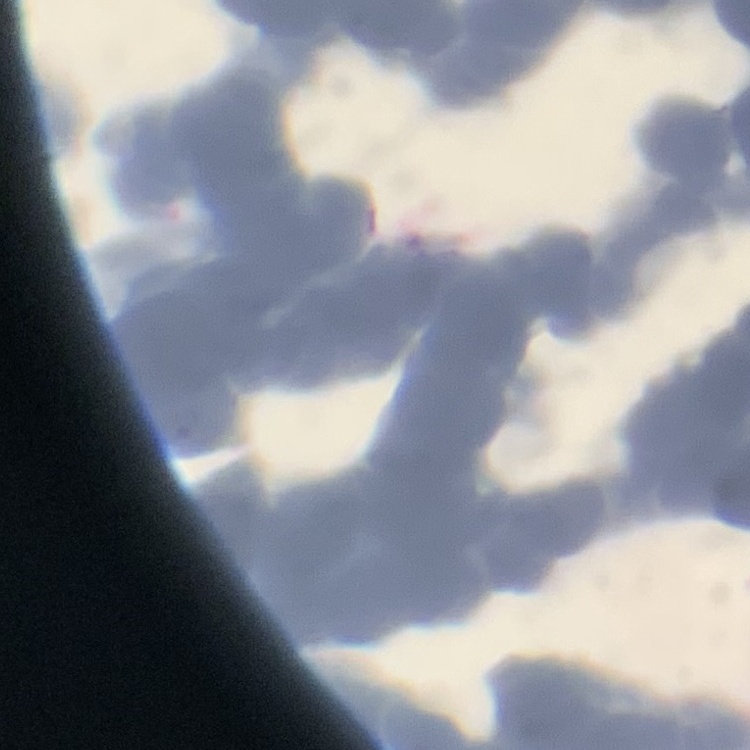

Summary:
  - Red blood cell morphology: rouleaux formation
  - Preparation: thin blood smear
  - Stain: Field's or Giemsa
  - Image type: one tile cut from a larger photomicrograph